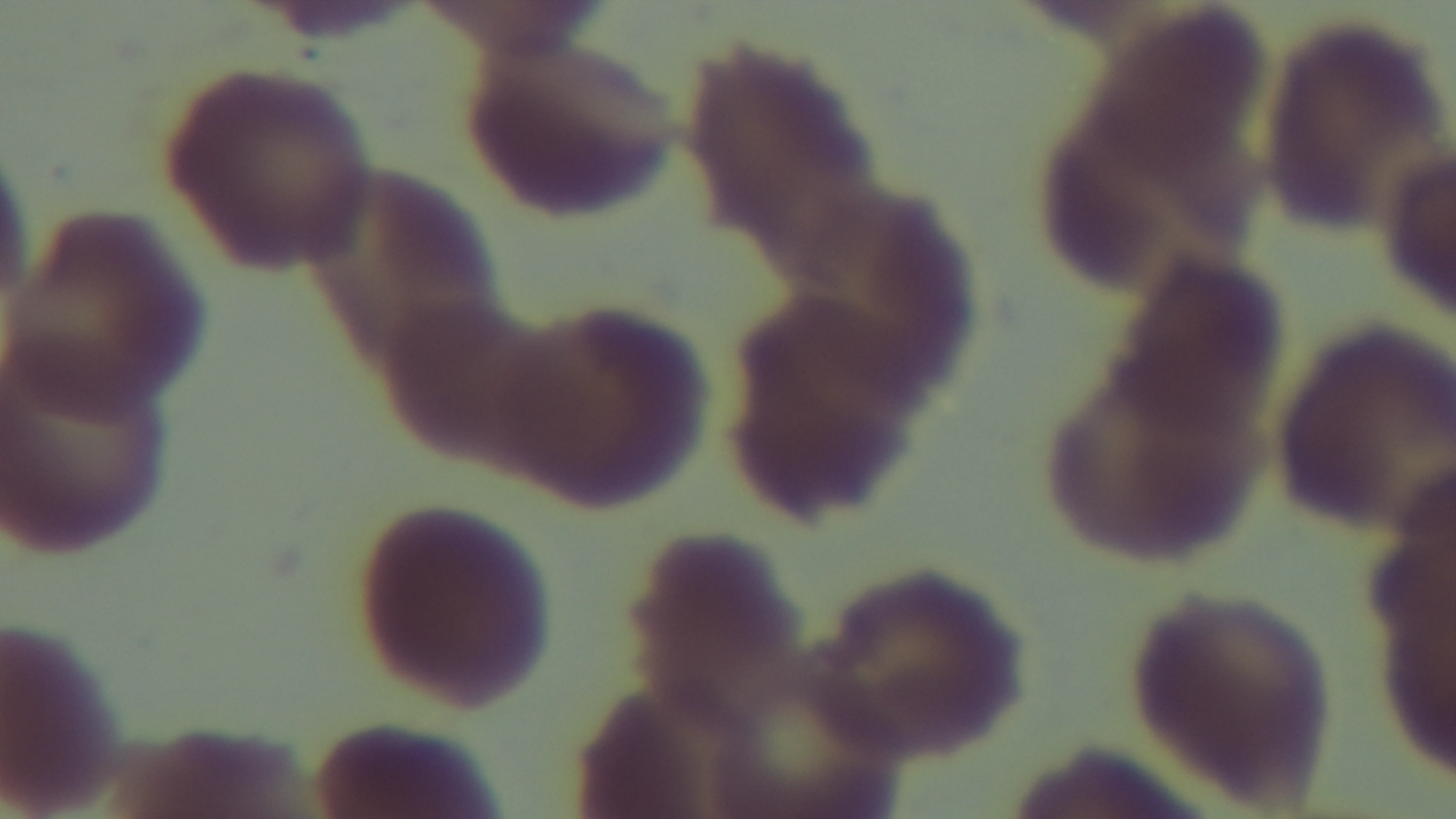

objective = 100x oil immersion
modality = light microscopy
preparation = thin smear
stain = Giemsa
field of view = single
malaria status = uninfected
capture = mounted 4K digital camera